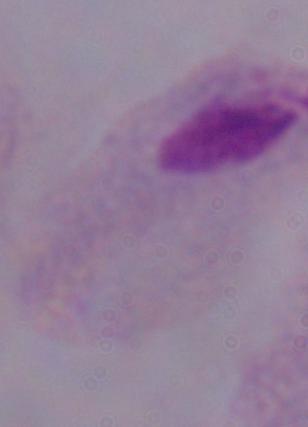
modality: photomicrograph
identification: trichomonad
magnification: 1000x